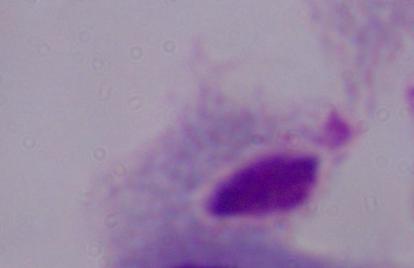
{
  "magnification": "1000x",
  "identification": "trichomonad",
  "modality": "micrograph"
}